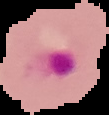

Result: Plasmodium parasites detected. Image is 109×115 pixels. From a thin blood smear. The area outside the segmented cell region is set to black.